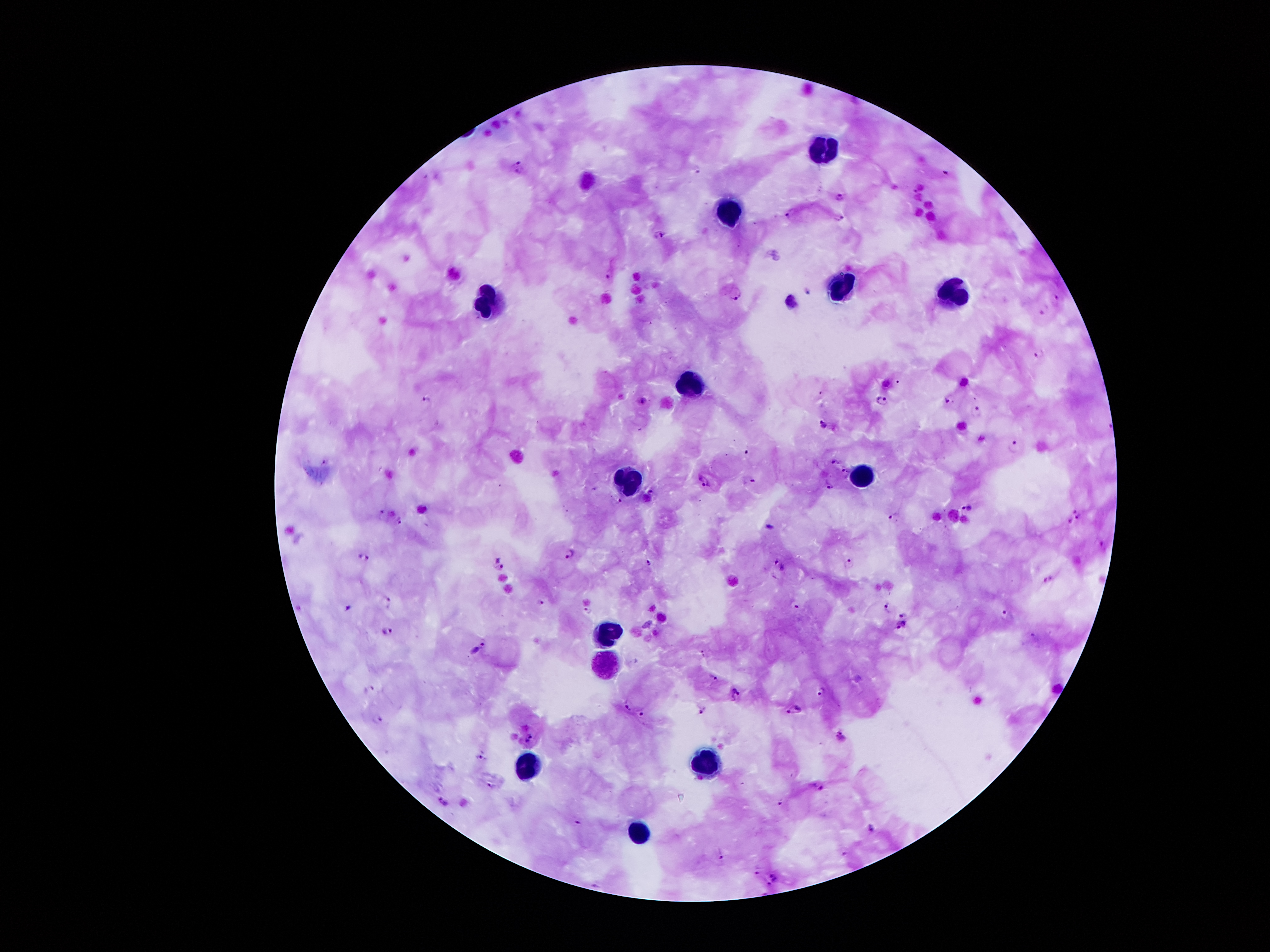
coordinate format = approximate centers as (x, y) in pixels
malaria parasite locations = (518, 166), (698, 169), (945, 174), (838, 198), (790, 215), (839, 218), (659, 235), (608, 275), (737, 294), (1055, 300), (1043, 311), (1037, 354), (426, 398), (950, 398), (643, 400), (883, 400), (975, 410), (822, 423), (1014, 444), (835, 460), (323, 461), (845, 471), (705, 480), (751, 481), (828, 485), (651, 494), (619, 500), (966, 507), (382, 514), (1077, 514), (895, 517), (398, 520), (768, 528), (567, 553), (367, 557), (648, 563), (848, 563), (499, 565), (780, 565), (1048, 579), (389, 602), (541, 603), (797, 603), (888, 606), (587, 609), (1006, 612), (903, 613), (900, 626), (388, 630), (1034, 637), (479, 647), (705, 653), (714, 677), (822, 691), (737, 694), (626, 704), (795, 708), (705, 709), (642, 712), (377, 719), (842, 735), (528, 737), (480, 757), (490, 786), (816, 786), (444, 802), (778, 802), (870, 828), (721, 854), (754, 873), (772, 876), (770, 885)
leukocyte locations = (821, 150), (730, 207), (837, 289), (948, 295), (489, 302), (688, 383), (861, 476), (622, 478), (607, 634), (604, 663), (709, 767), (522, 768), (638, 838)
patient malaria status = positive for Plasmodium falciparum
preparation = thick blood film
magnification = 100x
field of view = single
image size = 1270×952 pixels
capture = smartphone camera through the microscope eyepiece
stain = Giemsa